Report the malaria status of this cell.
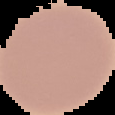
It is uninfected.

Summary:
  - Image type: segmented cell region on a black background
  - Image size: 115×115 pixels
  - Preparation: thin blood smear